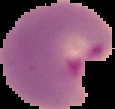

Image is 115×109 pixels. The area outside the segmented cell region is set to black. Malaria status: parasitized. From a thin blood smear.